Comment on the morphology of the red blood cells.
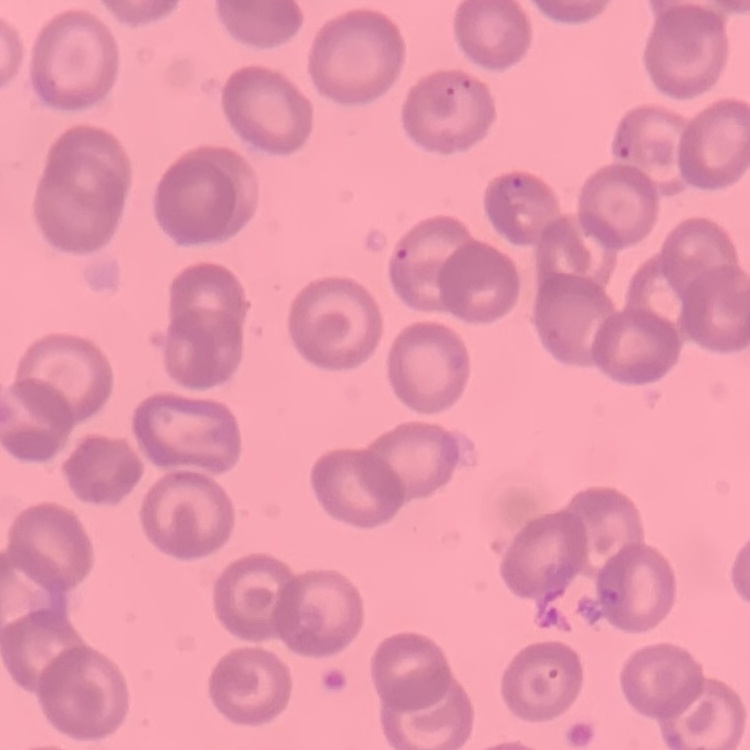
No rouleaux formation.

image type = one tile cut from a larger photomicrograph
stain = Field's or Giemsa
preparation = thin peripheral smear